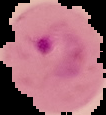 Image is 106×115 pixels. Result: Plasmodium parasites detected. Segmented cell region on a black background. From a thin blood smear.